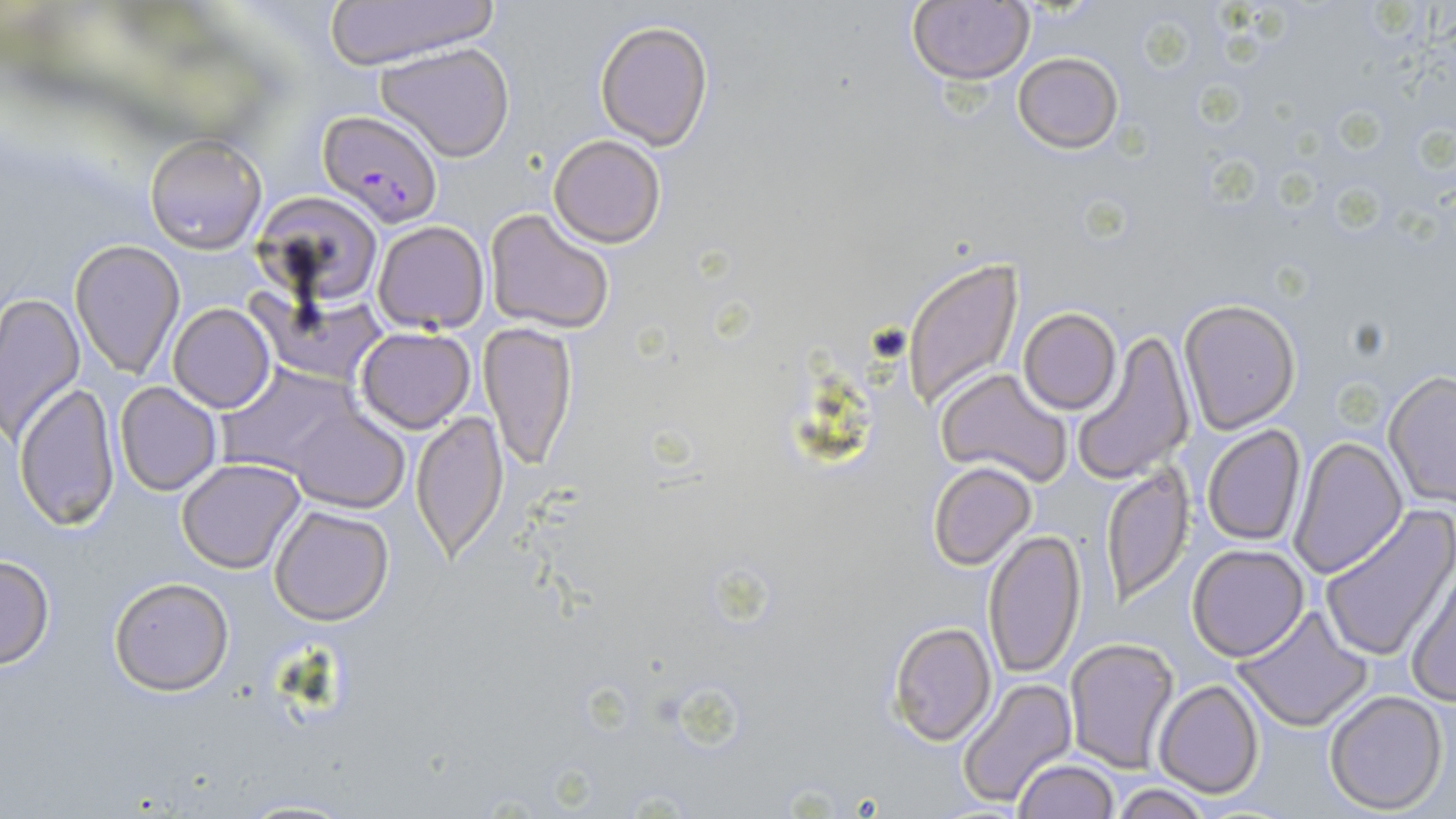

Approximate bounding boxes as named x1/y1/x2/y2 corners in pixels. Uninfected red blood cell locations: (x1=325, y1=1, x2=497, y2=67), (x1=909, y1=1, x2=1034, y2=84), (x1=595, y1=20, x2=714, y2=148), (x1=372, y1=42, x2=519, y2=164), (x1=1012, y1=52, x2=1124, y2=153), (x1=144, y1=134, x2=267, y2=253), (x1=548, y1=134, x2=666, y2=248), (x1=253, y1=193, x2=382, y2=306), (x1=482, y1=209, x2=616, y2=334), (x1=373, y1=220, x2=489, y2=332), (x1=69, y1=239, x2=185, y2=380), (x1=902, y1=256, x2=1025, y2=410), (x1=0, y1=291, x2=86, y2=443), (x1=256, y1=291, x2=388, y2=385), (x1=1178, y1=298, x2=1301, y2=435), (x1=168, y1=304, x2=276, y2=412), (x1=1019, y1=309, x2=1120, y2=414), (x1=479, y1=322, x2=576, y2=473), (x1=354, y1=326, x2=476, y2=433), (x1=1070, y1=329, x2=1194, y2=486), (x1=217, y1=364, x2=363, y2=479), (x1=937, y1=368, x2=1075, y2=487), (x1=1383, y1=372, x2=1456, y2=506), (x1=14, y1=382, x2=123, y2=530), (x1=115, y1=382, x2=221, y2=496), (x1=288, y1=407, x2=408, y2=513), (x1=411, y1=410, x2=509, y2=560), (x1=1202, y1=424, x2=1306, y2=546), (x1=1288, y1=435, x2=1406, y2=579), (x1=176, y1=458, x2=308, y2=573), (x1=927, y1=461, x2=1037, y2=570), (x1=1099, y1=465, x2=1193, y2=607), (x1=269, y1=504, x2=396, y2=625), (x1=1321, y1=504, x2=1456, y2=663), (x1=982, y1=529, x2=1086, y2=679), (x1=1186, y1=544, x2=1310, y2=661), (x1=0, y1=554, x2=54, y2=670), (x1=1405, y1=558, x2=1456, y2=705), (x1=108, y1=576, x2=236, y2=696), (x1=1233, y1=603, x2=1374, y2=732), (x1=887, y1=620, x2=997, y2=746), (x1=1063, y1=637, x2=1181, y2=774), (x1=953, y1=675, x2=1076, y2=809), (x1=1153, y1=679, x2=1265, y2=800), (x1=1323, y1=690, x2=1449, y2=814), (x1=1012, y1=759, x2=1120, y2=818), (x1=1108, y1=782, x2=1216, y2=818), (x1=232, y1=799, x2=363, y2=818). Plasmodium falciparum-infected red blood cell locations: (x1=317, y1=108, x2=445, y2=227). Slide-level diagnosis: Plasmodium falciparum. May-Grünwald-Giemsa stain. Image is 1456×819 pixels. 1000x magnification. Thin blood smear. Single field of view. Light microscopy.